Identify the parasite.
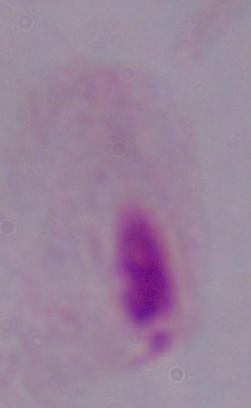
A trichomonad.

1000x magnification. Micrograph.